State which parasite is depicted.
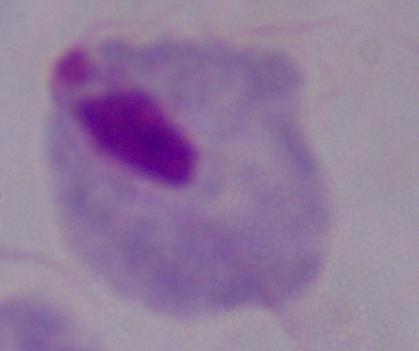
A trichomonad.

Summary:
  - Modality: micrograph
  - Magnification: 1000x